Report the malaria status of this cell.
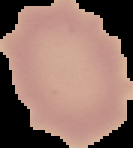
Uninfected.

Summary:
  - Image size: 133×148 pixels
  - Image type: segmented cell region on a black background
  - Preparation: thin blood film